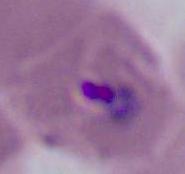
Summary:
  - Identification: Plasmodium
  - Modality: photomicrograph
  - Magnification: 400x or 1000x